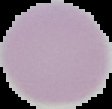
Segmented cell region on a black background. Result: no Plasmodium parasites detected. Image is 112×109 pixels. From a thin blood smear.